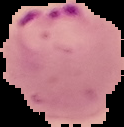

Segmented cell region on a black background. From a thin blood film. Malaria status: parasitized. Image is 124×127 pixels.